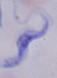

Summary:
  - Identification: trypanosome
  - Modality: micrograph
  - Magnification: 1000x